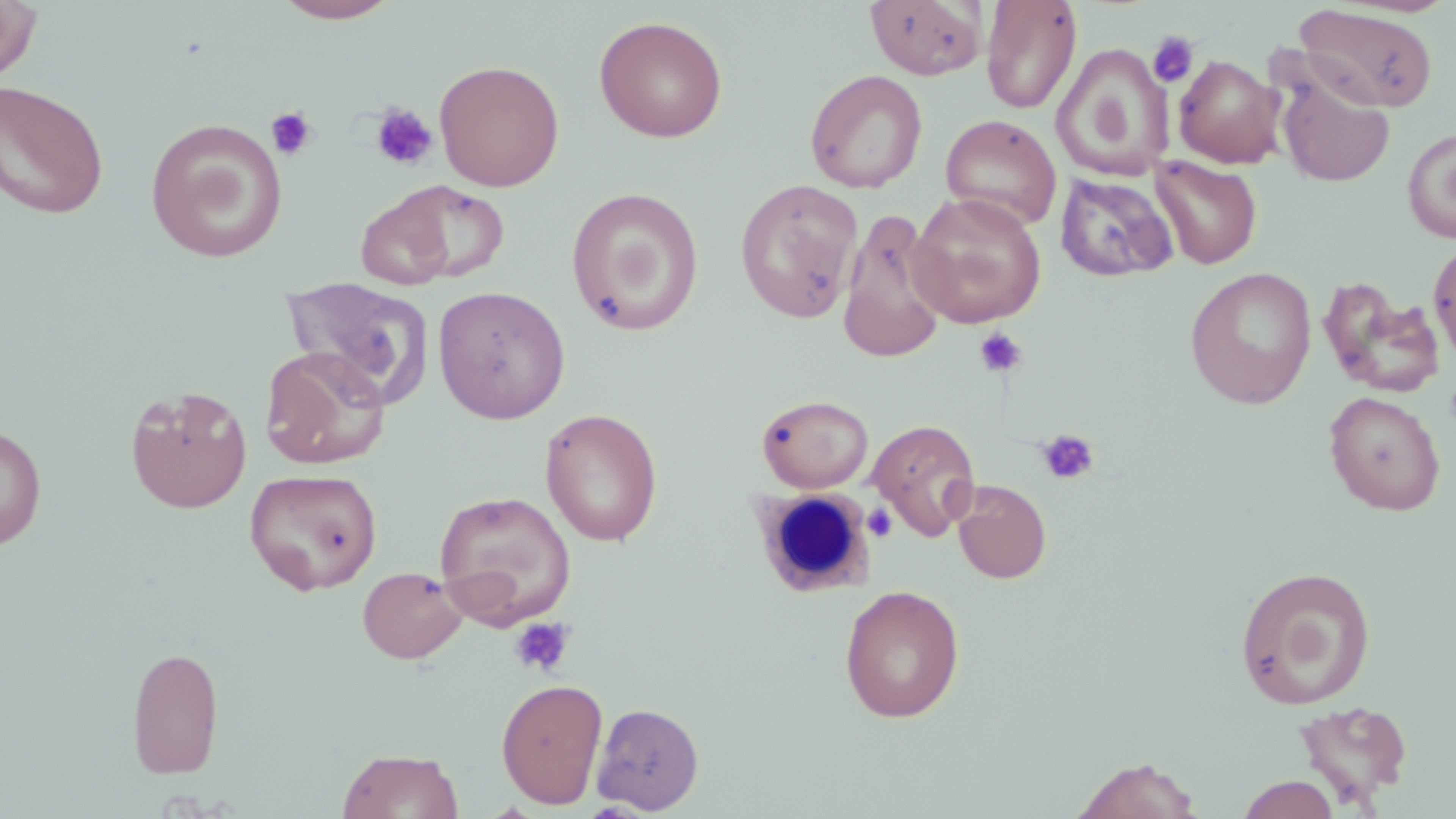

slide_level_diagnosis: negative for blood parasites
stain: May-Grünwald-Giemsa
platelet_locations: 'approximate bounding boxes as (x1,y1)-(x2,y2) corner pairs in pixels: (1148,31)-(1198,87), (370,103)-(438,171), (264,107)-(318,160), (973,327)-(1028,378), (1036,428)-(1100,486), (863,502)-(898,542), (509,616)-(574,677)'
modality: optical microscopy
magnification: 1000x
field_of_view: one of a larger specimen
image_size: 1456×819 pixels
white_blood_cell_locations: 'approximate bounding boxes as (x1,y1)-(x2,y2) corner pairs in pixels: (751,489)-(876,598)'
preparation: thin blood film
uninfected_red_blood_cell_locations: 'approximate bounding boxes as (x1,y1)-(x2,y2) corner pairs in pixels: (272,0)-(401,23), (0,1)-(42,83), (865,1)-(987,80), (980,1)-(1082,115), (1293,4)-(1439,113), (594,15)-(728,142), (1052,43)-(1175,180), (1174,54)-(1283,168), (433,60)-(565,191), (1274,68)-(1396,187), (805,69)-(928,193), (0,80)-(110,219), (940,114)-(1062,231), (145,119)-(288,262), (1402,125)-(1456,244), (1150,155)-(1262,269), (1056,173)-(1178,282), (735,178)-(864,324), (390,181)-(510,284), (566,186)-(705,335), (357,191)-(456,290), (908,192)-(1047,328), (838,208)-(949,362), (1428,238)-(1456,367), (1185,267)-(1318,409), (280,275)-(434,407), (1320,280)-(1446,398), (433,285)-(571,424), (259,346)-(390,470), (125,384)-(252,513), (1324,391)-(1446,515), (757,394)-(874,493), (540,408)-(663,546), (867,418)-(981,540), (0,423)-(47,551), (244,467)-(383,595), (953,480)-(1051,584), (434,490)-(576,629), (1235,564)-(1377,710), (357,566)-(468,664), (839,584)-(965,723), (126,645)-(224,780), (496,677)-(608,808), (1293,700)-(1414,808), (591,703)-(704,813), (337,748)-(464,819), (1070,756)-(1204,819), (1237,774)-(1340,819)'